Assess for malaria.
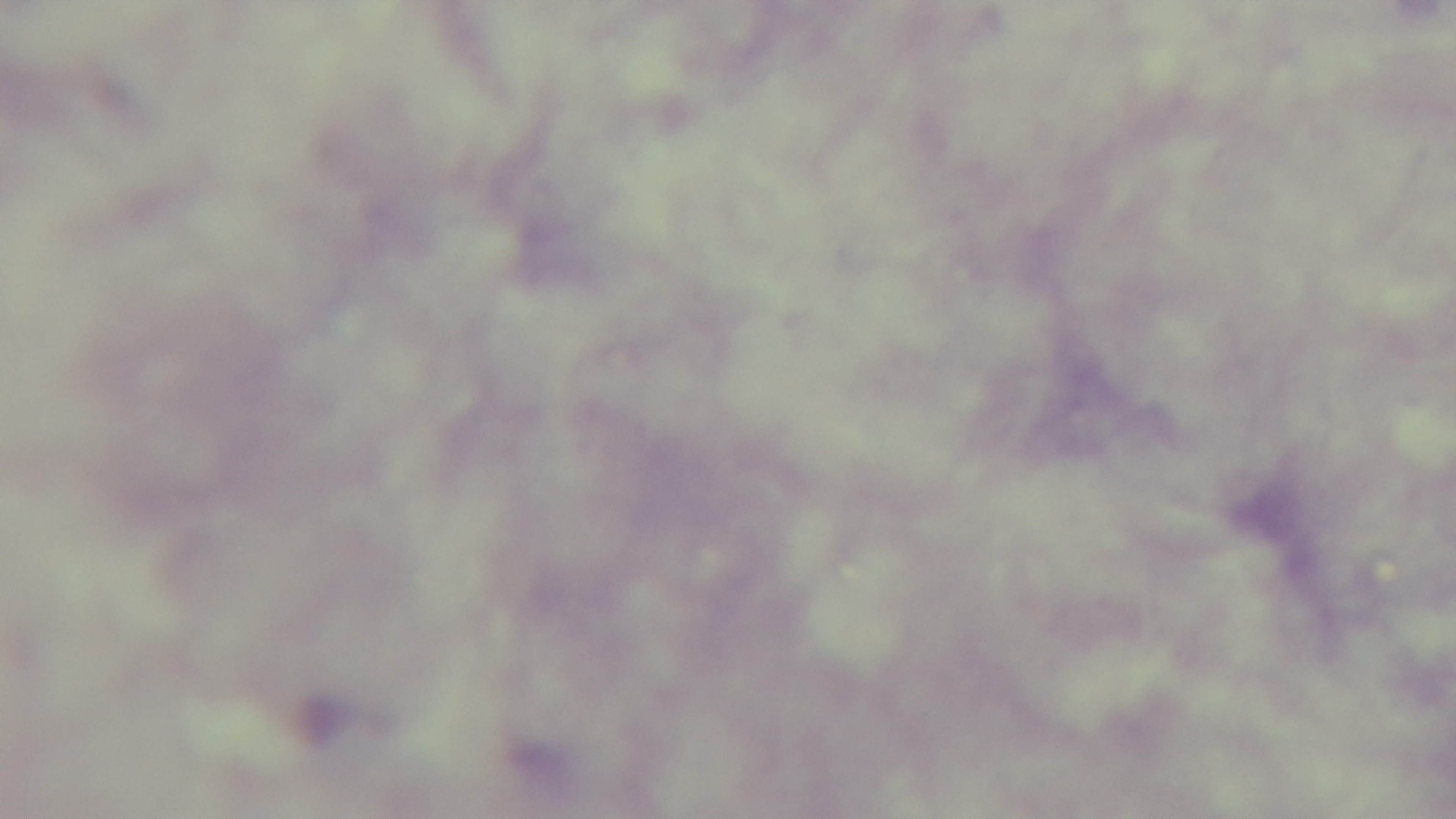
Uninfected.

capture = mounted 4K digital camera
preparation = thick blood film
modality = light microscopy
objective = 100x oil immersion
field of view = one from the slide
stain = Giemsa